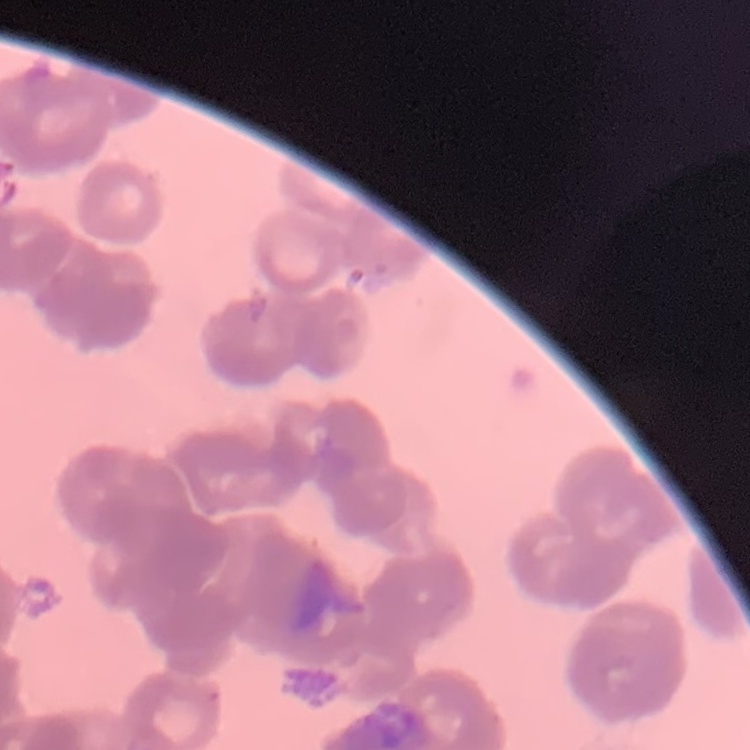

red_blood_cell_morphology: rouleaux formation
image_type: one tile cut from a larger photomicrograph
stain: Field's or Giemsa
preparation: thin blood smear